Assess the morphology of the erythrocytes.
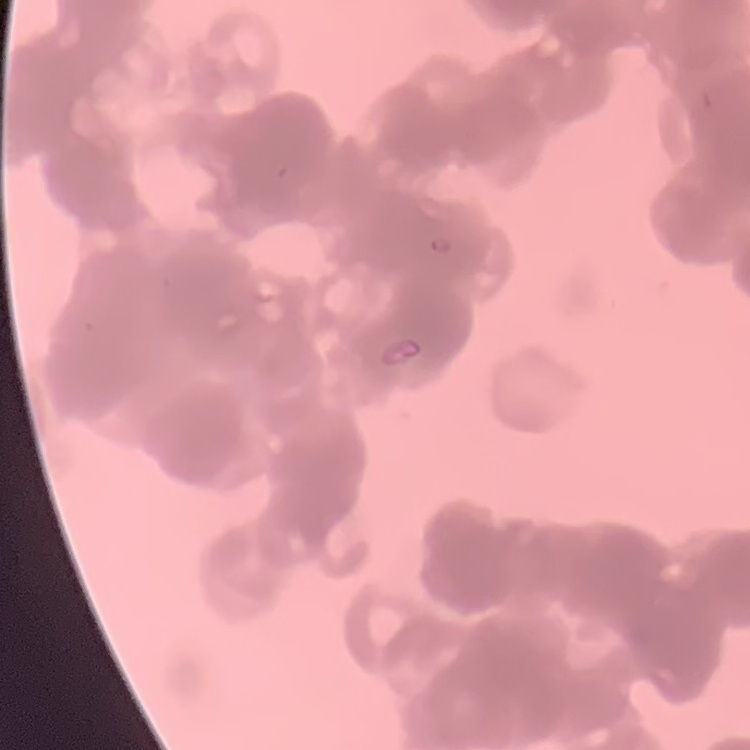
They show rouleaux formation.

Summary:
  - Preparation: thin peripheral smear
  - Image type: square crop of a larger photomicrograph
  - Stain: Field's or Giemsa